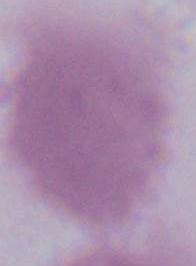
A red blood cell is shown. Micrograph. 1000x magnification.